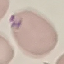

Summary:
  - Result: malaria parasites detected
  - Preparation: thin smear
  - Image type: cell patch, automatically extracted from a larger field of view and resized to 64 × 64 pixels
  - Stain: Giemsa
  - Capture: smartphone through the microscope eyepiece